State which parasite is depicted.
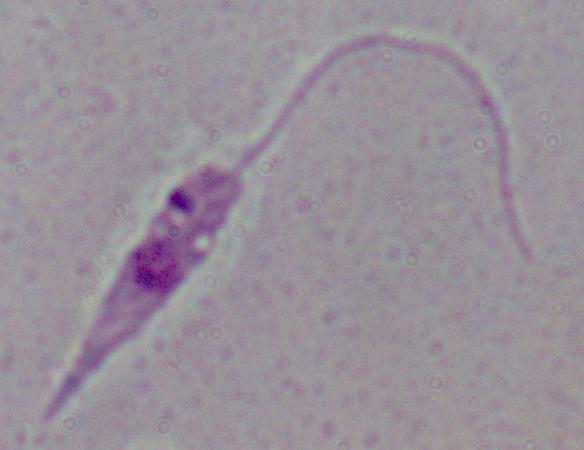
Leishmania.

1000x magnification. Micrograph.